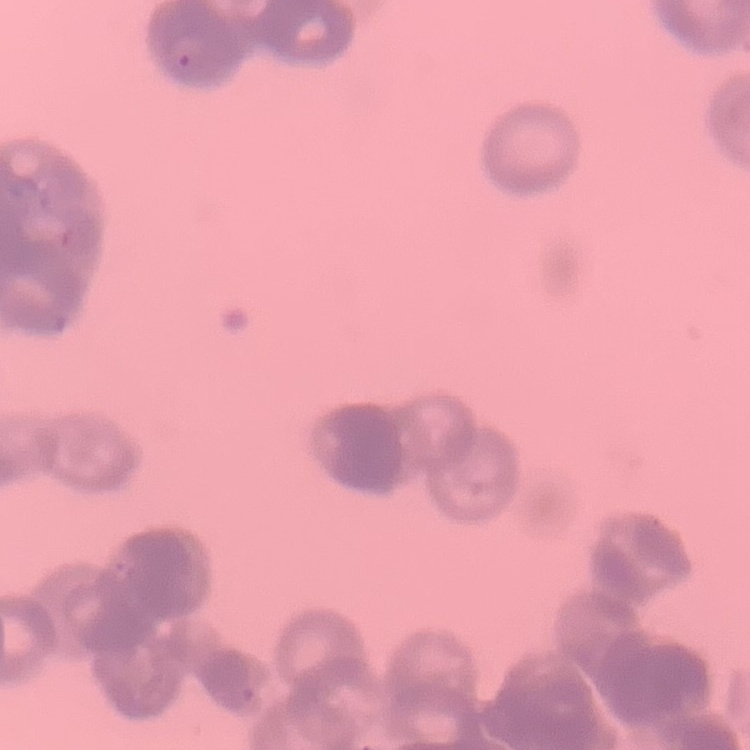

red blood cell morphology = rouleaux formation
image type = square crop of a larger photomicrograph
stain = Field's or Giemsa
preparation = thin blood film